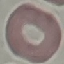
malaria status = uninfected
capture = smartphone through the microscope eyepiece
preparation = thin blood film
stain = Giemsa
image type = automatically extracted cell patch, resized to 64 × 64 pixels